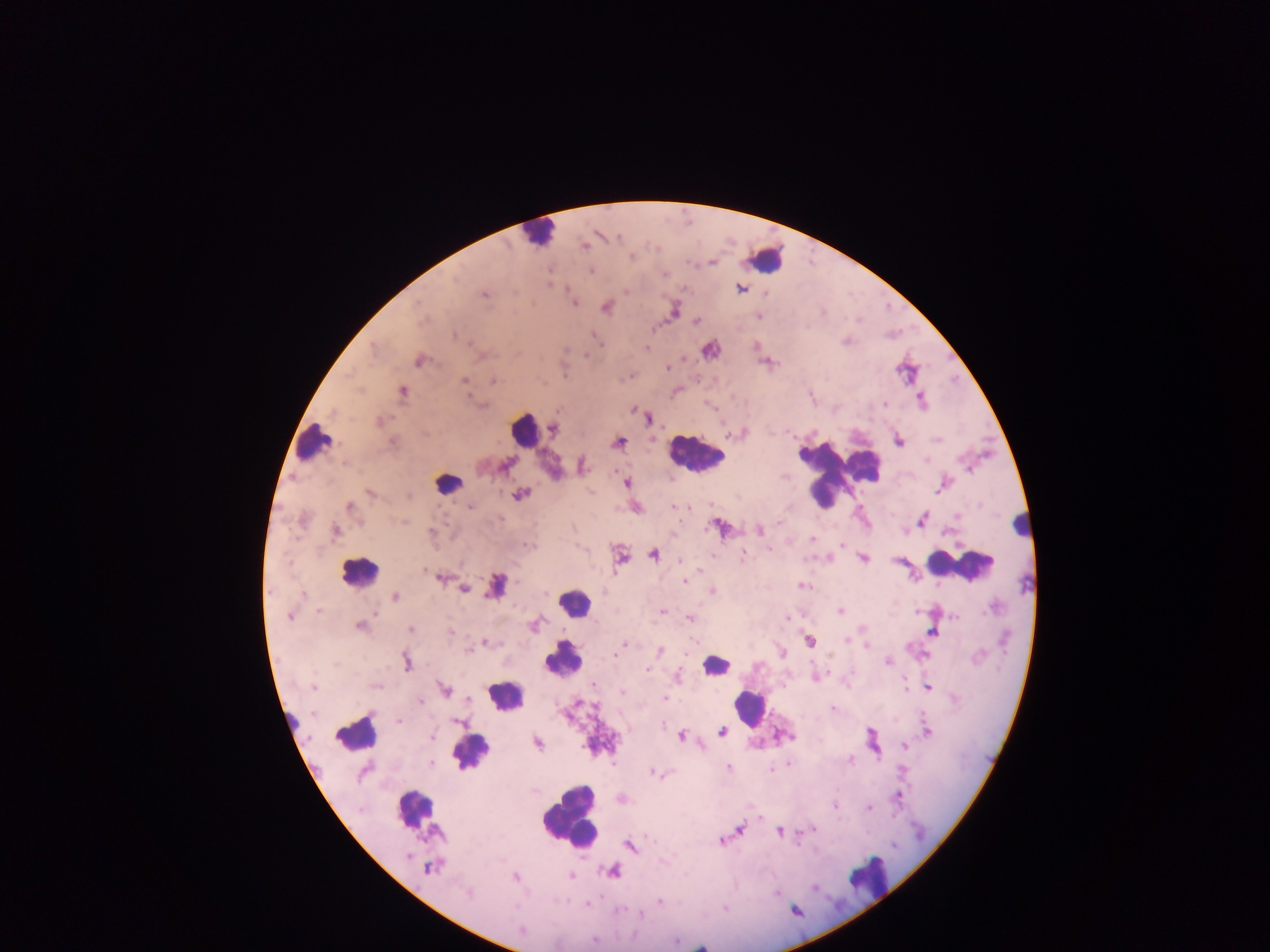

country = Ghana
malaria parasite locations = approximate centers as [x, y] in pixels: [617, 237], [585, 247], [632, 256], [591, 271], [665, 274], [741, 289], [626, 292], [483, 295], [417, 302], [574, 303], [605, 308], [758, 317], [697, 322], [455, 334], [600, 343], [647, 348], [420, 361], [668, 368], [464, 380], [493, 381], [403, 391], [884, 404], [481, 405], [649, 420], [379, 422], [555, 429], [900, 442], [619, 443], [505, 465], [582, 466], [626, 483], [370, 492], [521, 494], [409, 496], [675, 506], [351, 507], [470, 507], [957, 516], [922, 519], [404, 522], [759, 530], [336, 532], [431, 532], [812, 539], [842, 544], [528, 546], [743, 553], [653, 554], [713, 555], [862, 559], [681, 560], [424, 571], [440, 578], [685, 581], [801, 586], [464, 589], [712, 591], [303, 595], [396, 596], [318, 610], [662, 611], [840, 611], [290, 617], [955, 617], [690, 618], [786, 619], [360, 627], [411, 630], [451, 632], [933, 633], [847, 640], [810, 642], [486, 643], [623, 644], [867, 646], [660, 651], [467, 652], [616, 652], [781, 652], [615, 655], [406, 662], [888, 662], [337, 665], [646, 669], [593, 684], [313, 687], [375, 687], [928, 689], [445, 690], [622, 693], [665, 698], [468, 700], [421, 701], [832, 708], [399, 721], [457, 722], [927, 731], [722, 732], [431, 737], [681, 737], [538, 743], [702, 746], [904, 747], [431, 763], [789, 764], [728, 767], [364, 772], [653, 773], [898, 797], [835, 806], [868, 808], [760, 818], [741, 829], [814, 829], [781, 832], [721, 841], [630, 848], [408, 856], [429, 869], [613, 871], [516, 877], [572, 877], [815, 888], [467, 894], [659, 902], [587, 905], [641, 915], [521, 930], [594, 940], [701, 947]
leukocyte locations = approximate centers as [x, y] in pixels: [538, 227], [766, 256], [524, 428], [315, 443], [695, 457], [834, 473], [822, 481], [447, 483], [1023, 524], [960, 565], [358, 571], [497, 583], [575, 601], [563, 661], [715, 664], [503, 696], [749, 708], [288, 718], [355, 732], [473, 749], [415, 810], [570, 817], [872, 883]
capture = mobile-phone photograph through a microscope
image size = 1270×952 pixels
field of view = single
preparation = thick blood film